Identify the parasite.
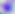
Toxoplasma gondii.

400x magnification. Photomicrograph.